Report the malaria status of this cell.
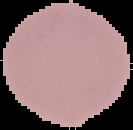
Uninfected.

Summary:
  - Image size: 133×130 pixels
  - Preparation: thin blood smear
  - Image type: cell region segmented out of the field of view; surrounding area masked to black